Give the position of every leukocyte visible.
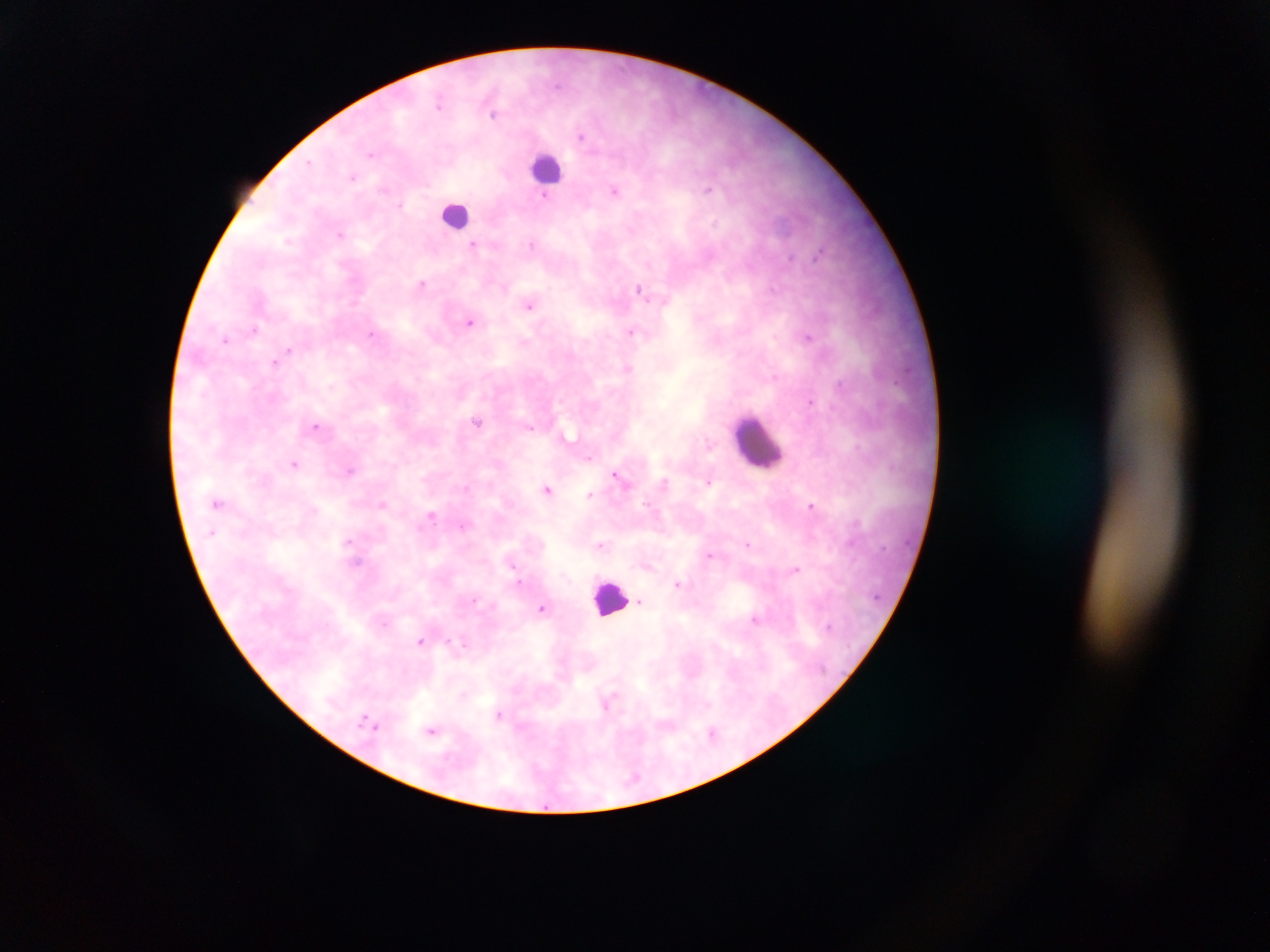
Approximate centers as x y in pixels.
Leukocytes: 547 168; 455 215; 758 443; 610 598.

preparation: thick blood film
image_size: 1270×952 pixels
plasmodium_parasite_locations: 'approximate centers as x y in pixels: 495 114; 583 137; 353 177; 708 188; 616 189; 545 194; 474 245; 423 283; 640 290; 530 305; 471 321; 255 329; 631 332; 371 334; 808 336; 227 337; 289 350; 274 361; 628 369; 477 420; 316 426; 529 427; 710 444; 591 456; 295 464; 351 470; 620 476; 708 479; 549 489; 590 494; 219 503; 382 504; 813 505; 432 515; 348 541; 749 543; 602 544; 710 554; 795 568; 521 583; 680 584; 641 600; 543 608; 757 618; 421 641; 463 643; 608 702; 500 714; 432 730; 713 733'
country: Ghana
capture: mobile-phone photograph through a microscope
field_of_view: single